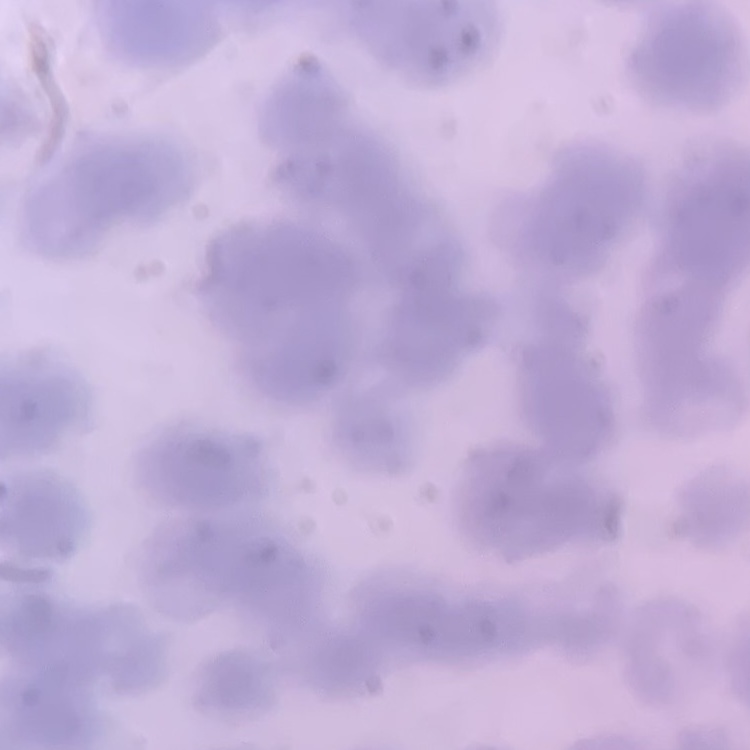
Summary:
  - Red blood cell morphology: rouleaux formation
  - Stain: Field's or Giemsa
  - Image type: square crop of a larger photomicrograph
  - Preparation: thin blood film